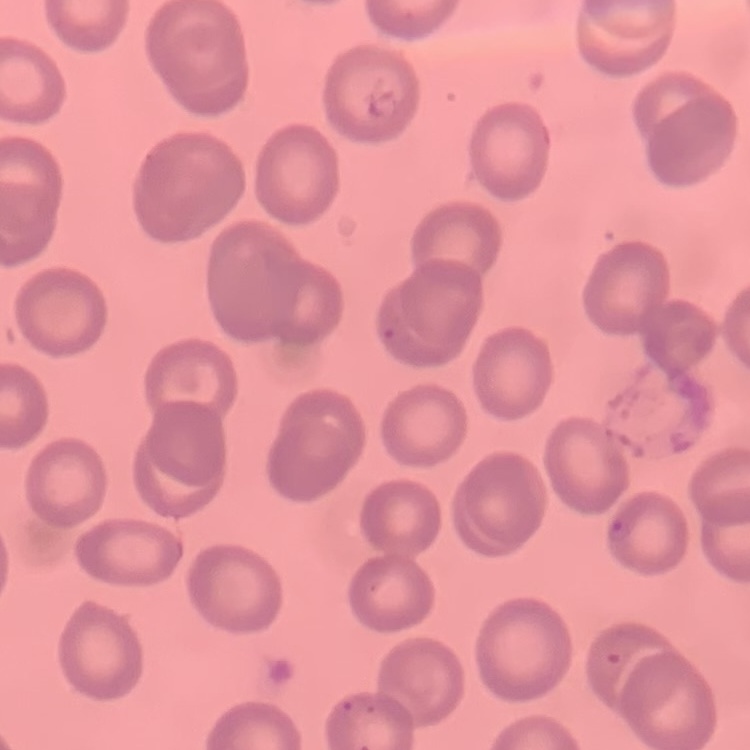
Summary:
  - Red blood cell morphology: no rouleaux formation
  - Stain: Field's or Giemsa
  - Preparation: thin blood smear
  - Image type: one tile cut from a larger photomicrograph